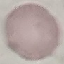
result = no malaria parasites seen
preparation = thin blood film
capture = smartphone through the microscope eyepiece
image type = cell patch, automatically extracted from a larger field of view and resized to 64 × 64 pixels
stain = Giemsa